Locate platelets.
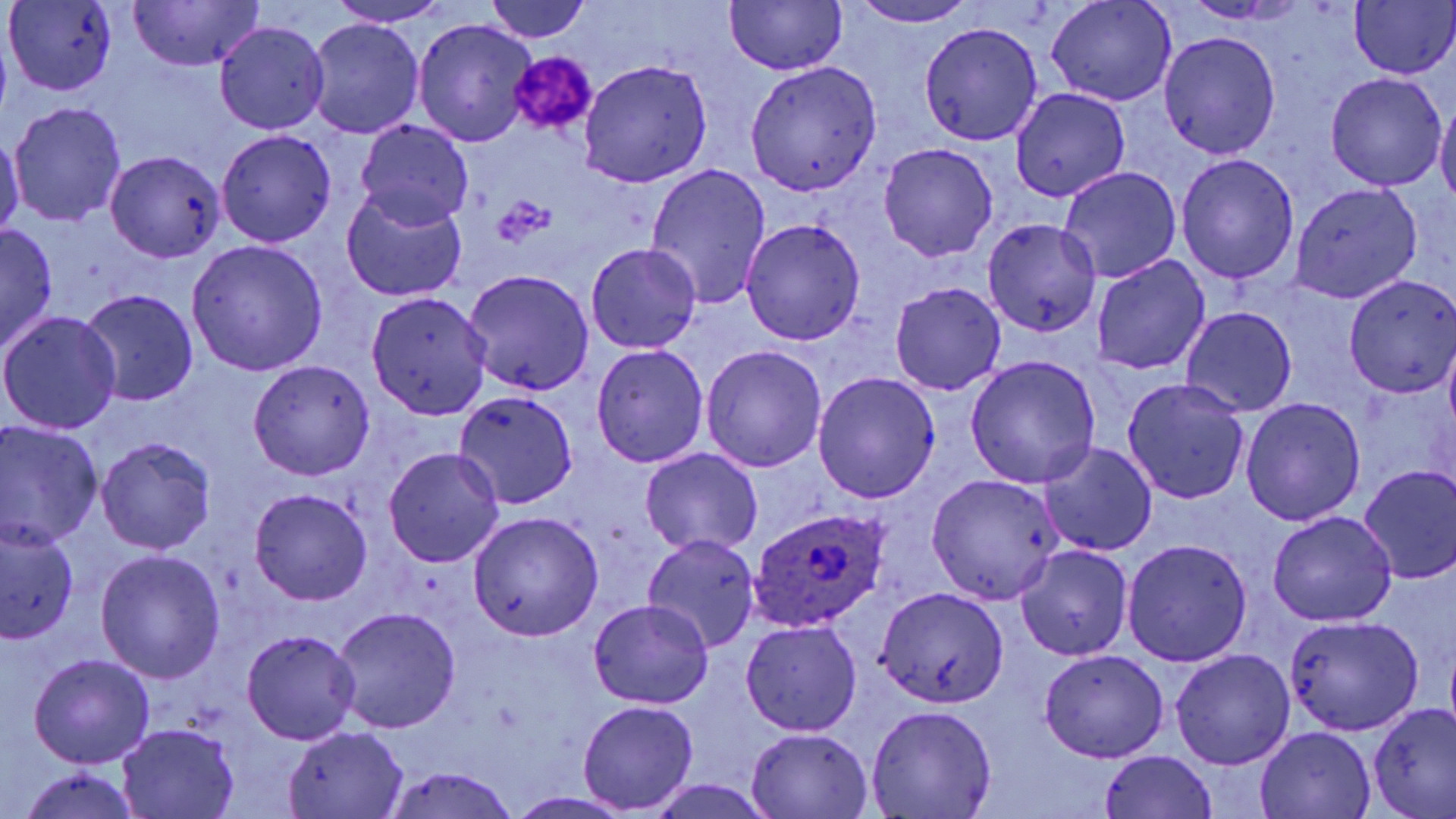
Approximate bounding boxes as named x1/y1/x2/y2 corners in pixels.
Platelets: (x1=509, y1=51, x2=597, y2=133), (x1=492, y1=195, x2=556, y2=248).

Uninfected red blood cell locations: (x1=128, y1=0, x2=263, y2=73), (x1=724, y1=0, x2=848, y2=75), (x1=1045, y1=0, x2=1174, y2=105), (x1=1350, y1=0, x2=1456, y2=81), (x1=4, y1=1, x2=118, y2=95), (x1=327, y1=1, x2=456, y2=26), (x1=481, y1=1, x2=595, y2=44), (x1=849, y1=1, x2=979, y2=26), (x1=306, y1=18, x2=424, y2=139), (x1=214, y1=22, x2=329, y2=134), (x1=413, y1=22, x2=534, y2=145), (x1=920, y1=22, x2=1043, y2=145), (x1=1159, y1=31, x2=1281, y2=159), (x1=578, y1=60, x2=714, y2=187), (x1=744, y1=61, x2=883, y2=195), (x1=1325, y1=71, x2=1447, y2=191), (x1=1009, y1=88, x2=1131, y2=202), (x1=1436, y1=97, x2=1456, y2=210), (x1=7, y1=102, x2=127, y2=225), (x1=356, y1=120, x2=474, y2=230), (x1=216, y1=130, x2=337, y2=247), (x1=0, y1=132, x2=25, y2=242), (x1=878, y1=143, x2=997, y2=262), (x1=107, y1=149, x2=227, y2=264), (x1=1175, y1=153, x2=1299, y2=287), (x1=644, y1=164, x2=772, y2=307), (x1=1058, y1=167, x2=1182, y2=281), (x1=1290, y1=181, x2=1424, y2=303), (x1=341, y1=188, x2=469, y2=303), (x1=741, y1=218, x2=865, y2=345), (x1=983, y1=218, x2=1102, y2=337), (x1=1, y1=224, x2=60, y2=355), (x1=187, y1=241, x2=328, y2=376), (x1=586, y1=242, x2=700, y2=352), (x1=1091, y1=253, x2=1211, y2=377), (x1=462, y1=270, x2=594, y2=396), (x1=1344, y1=272, x2=1456, y2=396), (x1=889, y1=281, x2=1005, y2=395), (x1=78, y1=287, x2=200, y2=408), (x1=366, y1=292, x2=494, y2=418), (x1=1180, y1=306, x2=1297, y2=417), (x1=1, y1=310, x2=122, y2=434), (x1=1443, y1=339, x2=1456, y2=445), (x1=591, y1=344, x2=709, y2=469), (x1=702, y1=345, x2=826, y2=469), (x1=963, y1=355, x2=1101, y2=488), (x1=248, y1=359, x2=376, y2=480), (x1=812, y1=371, x2=941, y2=501), (x1=1122, y1=378, x2=1250, y2=504), (x1=453, y1=391, x2=580, y2=509), (x1=1240, y1=397, x2=1365, y2=526), (x1=0, y1=423, x2=102, y2=548), (x1=96, y1=436, x2=216, y2=553), (x1=1039, y1=442, x2=1157, y2=556), (x1=384, y1=447, x2=504, y2=568), (x1=640, y1=448, x2=763, y2=559), (x1=1358, y1=465, x2=1456, y2=584), (x1=926, y1=474, x2=1063, y2=604), (x1=250, y1=489, x2=372, y2=606), (x1=1267, y1=509, x2=1398, y2=626), (x1=468, y1=511, x2=604, y2=641), (x1=0, y1=521, x2=78, y2=644), (x1=642, y1=533, x2=762, y2=654), (x1=1123, y1=537, x2=1254, y2=667), (x1=1015, y1=543, x2=1133, y2=662), (x1=95, y1=551, x2=226, y2=683), (x1=874, y1=588, x2=1009, y2=707), (x1=589, y1=600, x2=713, y2=710), (x1=331, y1=606, x2=461, y2=735), (x1=1282, y1=613, x2=1425, y2=737), (x1=741, y1=620, x2=861, y2=735), (x1=242, y1=631, x2=360, y2=745), (x1=1037, y1=649, x2=1170, y2=763), (x1=1169, y1=649, x2=1295, y2=770), (x1=28, y1=653, x2=154, y2=769), (x1=578, y1=700, x2=699, y2=814), (x1=1368, y1=703, x2=1456, y2=818), (x1=866, y1=704, x2=998, y2=818), (x1=116, y1=726, x2=239, y2=817), (x1=283, y1=727, x2=409, y2=818), (x1=744, y1=727, x2=875, y2=819), (x1=1254, y1=728, x2=1375, y2=818), (x1=1098, y1=750, x2=1221, y2=819), (x1=383, y1=765, x2=520, y2=819), (x1=14, y1=766, x2=145, y2=819), (x1=642, y1=779, x2=780, y2=819), (x1=505, y1=793, x2=636, y2=818). Plasmodium ovale-infected red blood cell locations: (x1=749, y1=504, x2=886, y2=632). Slide-level diagnosis: Plasmodium ovale. May-Grünwald-Giemsa-stained preparation. Thin blood film. One field of a larger specimen. Captured at 1000x magnification. Image is 1456×819 pixels. Optical microscopy.